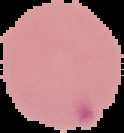
Summary:
  - Result: Plasmodium parasites identified
  - Image type: segmented cell region with the area outside set to black
  - Preparation: thin blood smear
  - Image size: 124×133 pixels